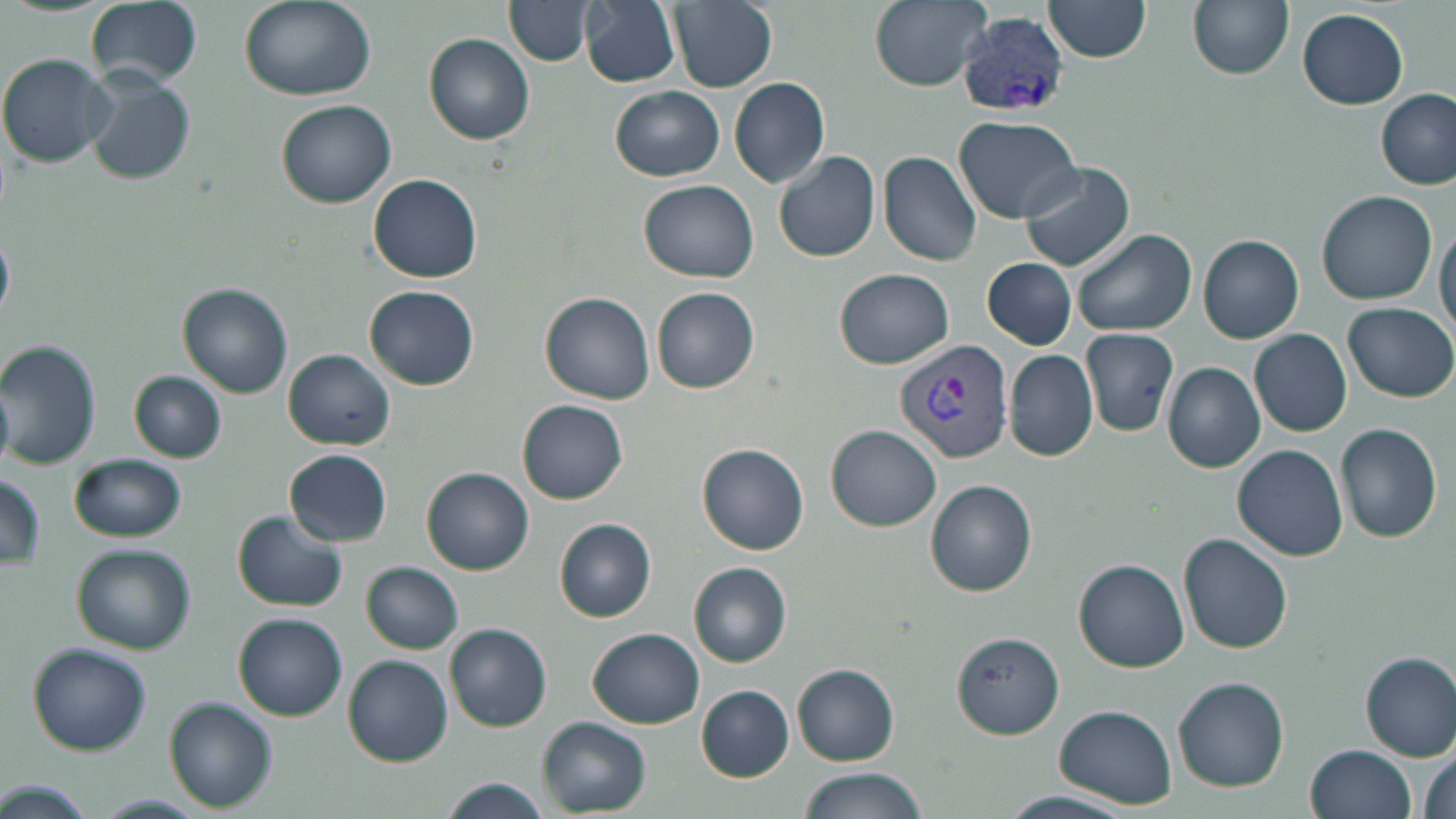
Approximate bounding boxes as (x1,y1)-(x2,y2) corner pairs in pixels. Plasmodium vivax-infected red blood cell locations: (956,13)-(1068,117), (894,340)-(1016,463). Uninfected red blood cell locations: (84,0)-(205,89), (583,0)-(679,86), (670,0)-(778,91), (869,0)-(991,90), (1188,0)-(1293,79), (238,1)-(376,102), (508,1)-(594,64), (1044,1)-(1153,64), (1298,7)-(1407,109), (425,35)-(535,144), (0,53)-(115,168), (85,70)-(195,185), (729,76)-(829,186), (611,86)-(725,180), (1376,90)-(1455,191), (277,99)-(396,206), (955,115)-(1083,223), (773,149)-(880,262), (879,151)-(982,266), (1019,161)-(1135,273), (368,174)-(483,283), (640,181)-(761,282), (1318,190)-(1437,305), (1436,219)-(1456,341), (1074,229)-(1198,337), (1198,233)-(1305,344), (0,234)-(13,320), (982,257)-(1078,350), (835,269)-(954,369), (178,285)-(293,399), (365,286)-(479,390), (652,287)-(760,394), (540,291)-(655,404), (1345,301)-(1455,401), (1080,328)-(1180,437), (1250,329)-(1352,435), (0,339)-(102,469), (1004,348)-(1098,462), (285,349)-(394,449), (1163,362)-(1264,471), (132,370)-(226,462), (518,399)-(628,504), (1336,424)-(1443,544), (825,425)-(941,531), (697,443)-(808,555), (1233,444)-(1348,561), (285,449)-(394,545), (71,453)-(186,542), (423,468)-(533,575), (0,473)-(46,572), (926,480)-(1038,596), (232,511)-(348,612), (555,518)-(657,622), (1180,533)-(1292,653), (74,543)-(195,654), (1073,559)-(1190,672), (363,561)-(464,653), (689,562)-(791,668), (234,614)-(348,720), (446,623)-(551,731), (589,628)-(703,726), (952,630)-(1064,736), (28,644)-(151,757), (1360,652)-(1456,760), (344,654)-(453,766), (793,664)-(898,764), (1174,677)-(1289,792), (697,686)-(794,781), (164,699)-(278,811), (1055,705)-(1179,808), (537,718)-(651,814), (1306,744)-(1417,819), (1415,746)-(1456,819), (795,768)-(929,819), (436,777)-(553,819), (1,779)-(97,819), (997,789)-(1137,818), (92,793)-(205,817). Slide-level diagnosis: Plasmodium vivax. One field of a larger specimen. May-Grünwald-Giemsa-stained preparation. Thin blood film. Image is 1456×819 pixels. 1000x magnification. Optical microscopy.